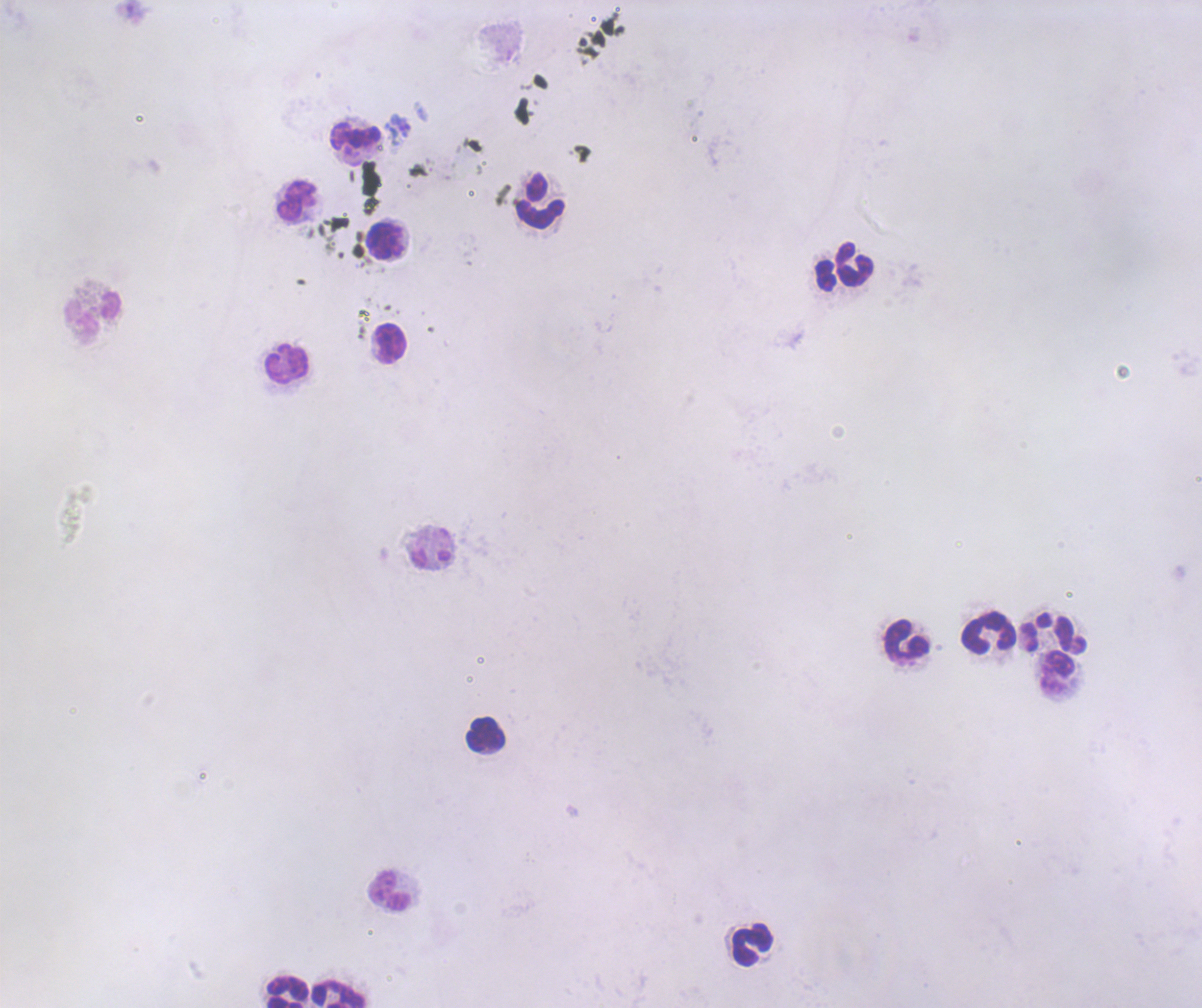
Approximate object centers, in pixels from the top-left corner. Leukocyte locations: (x=356, y=135), (x=296, y=201), (x=541, y=201), (x=384, y=240), (x=854, y=265), (x=92, y=319), (x=390, y=344), (x=286, y=364), (x=987, y=634), (x=905, y=640), (x=1057, y=673), (x=486, y=734), (x=390, y=891), (x=751, y=946), (x=287, y=992), (x=338, y=994). Coloration quality: bad. Single field of view. Thick smear of blood. Previously used in an actual diagnosis. Captured at 100x magnification. Background quality: poor. Result: no malaria parasites detected. Romanowsky-stained preparation. Image is 1202×1008 pixels.